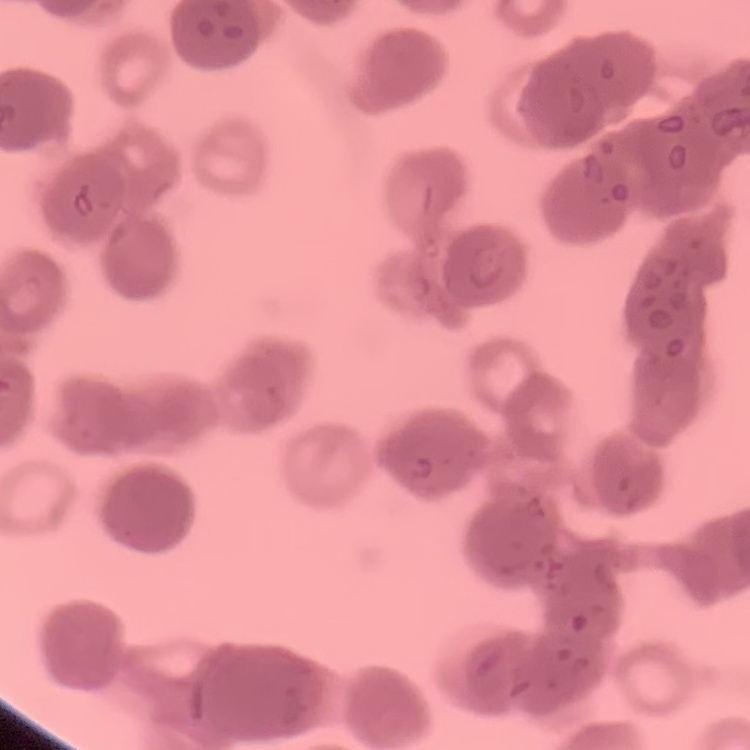
The red blood cells exhibit rouleaux formation. Thin peripheral smear. One tile cut from a larger photomicrograph. Field's or Giemsa stain.